Locate every blood parasite and identify its species.
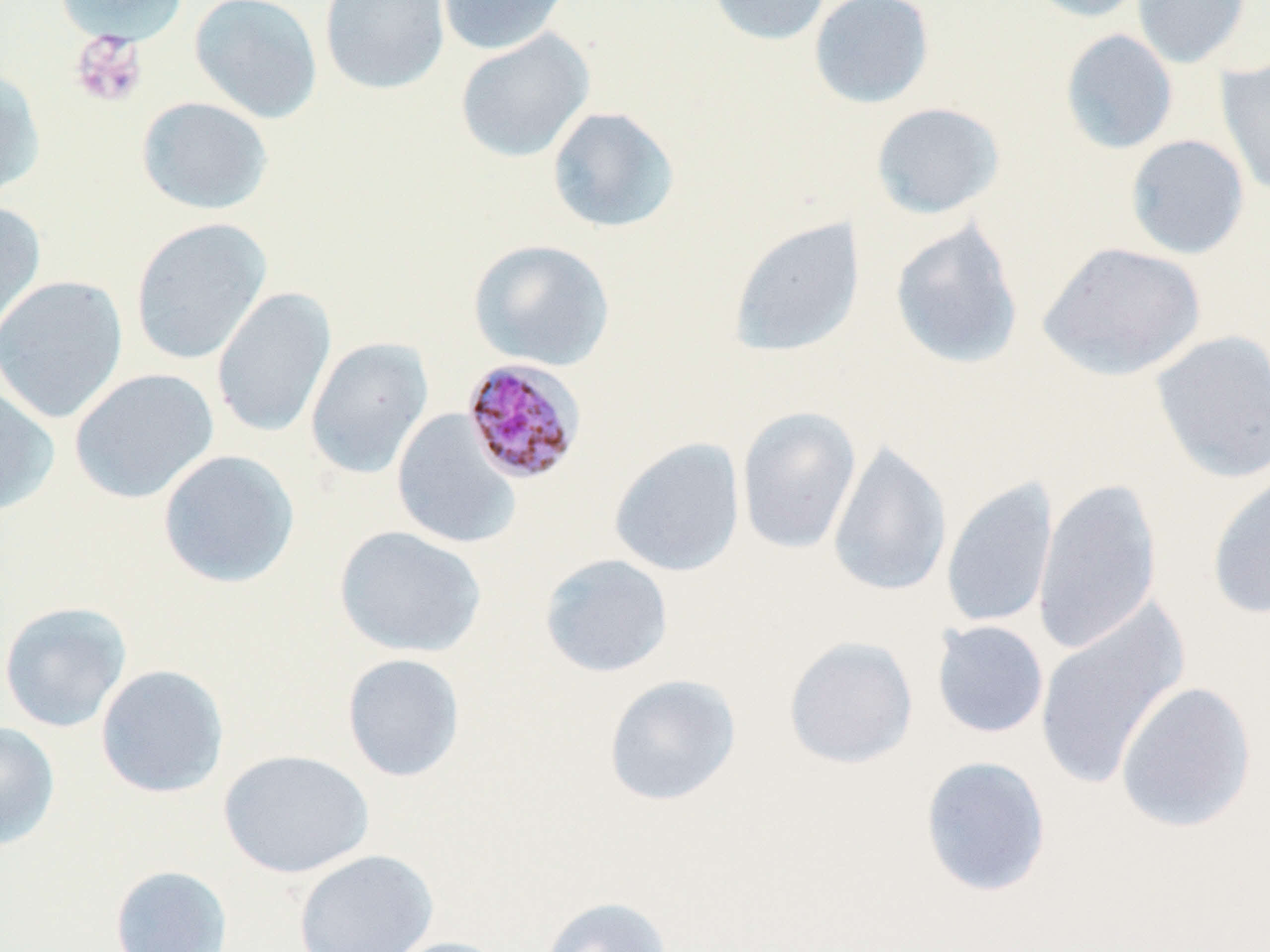

Approximate bounding boxes as (x1, y1, x2, y2) in pixels.
Plasmodium malariae-infected red blood cells: (461, 358, 587, 486).
No Plasmodium falciparum, Plasmodium ovale, Plasmodium vivax, Babesia divergens, or Trypanosoma brucei observed.

Uninfected red blood cell locations: (54, 0, 189, 46), (189, 0, 323, 124), (318, 0, 450, 95), (436, 0, 572, 56), (705, 0, 833, 46), (808, 0, 936, 110), (1022, 0, 1150, 23), (1132, 0, 1253, 69), (454, 28, 595, 163), (1059, 29, 1179, 155), (1216, 55, 1270, 199), (0, 67, 47, 202), (136, 96, 274, 215), (870, 101, 1006, 220), (546, 105, 681, 235), (1125, 134, 1250, 260), (0, 200, 46, 346), (129, 217, 272, 365), (727, 217, 866, 358), (889, 218, 1024, 370), (467, 238, 616, 371), (1036, 241, 1207, 382), (0, 274, 129, 424), (211, 287, 337, 438), (1150, 329, 1270, 483), (304, 336, 435, 480), (68, 367, 220, 504), (0, 382, 60, 516), (736, 405, 862, 554), (391, 409, 522, 550), (608, 437, 746, 577), (826, 440, 952, 598), (156, 449, 301, 589), (1206, 471, 1270, 619), (941, 477, 1059, 630), (1032, 477, 1163, 655), (334, 525, 487, 658), (538, 553, 674, 679), (0, 600, 133, 733), (1033, 601, 1190, 791), (931, 620, 1049, 739), (783, 634, 919, 770), (341, 652, 466, 783), (95, 664, 230, 799), (602, 673, 742, 807), (1115, 680, 1257, 834), (0, 720, 61, 852), (217, 748, 374, 879), (919, 755, 1053, 898), (293, 848, 439, 952), (109, 864, 233, 952), (537, 895, 675, 952), (381, 936, 518, 952). Platelet locations: (70, 31, 147, 108). Slide-level diagnosis: Plasmodium malariae. Image is 1270×952 pixels. Thin blood smear. May-Grünwald-Giemsa-stained preparation. Light microscopy. 1000x magnification. Single field of view.